Assess this cell for malaria.
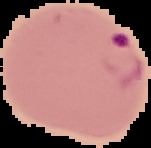

It is parasitized.

image size = 151×148 pixels
image type = cell region segmented out of the field of view; surrounding area masked to black
preparation = thin blood film